Assess this cell for malaria.
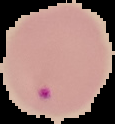
Parasitized.

Image is 115×124 pixels. From a thin blood smear. The area outside the segmented cell region is set to black.